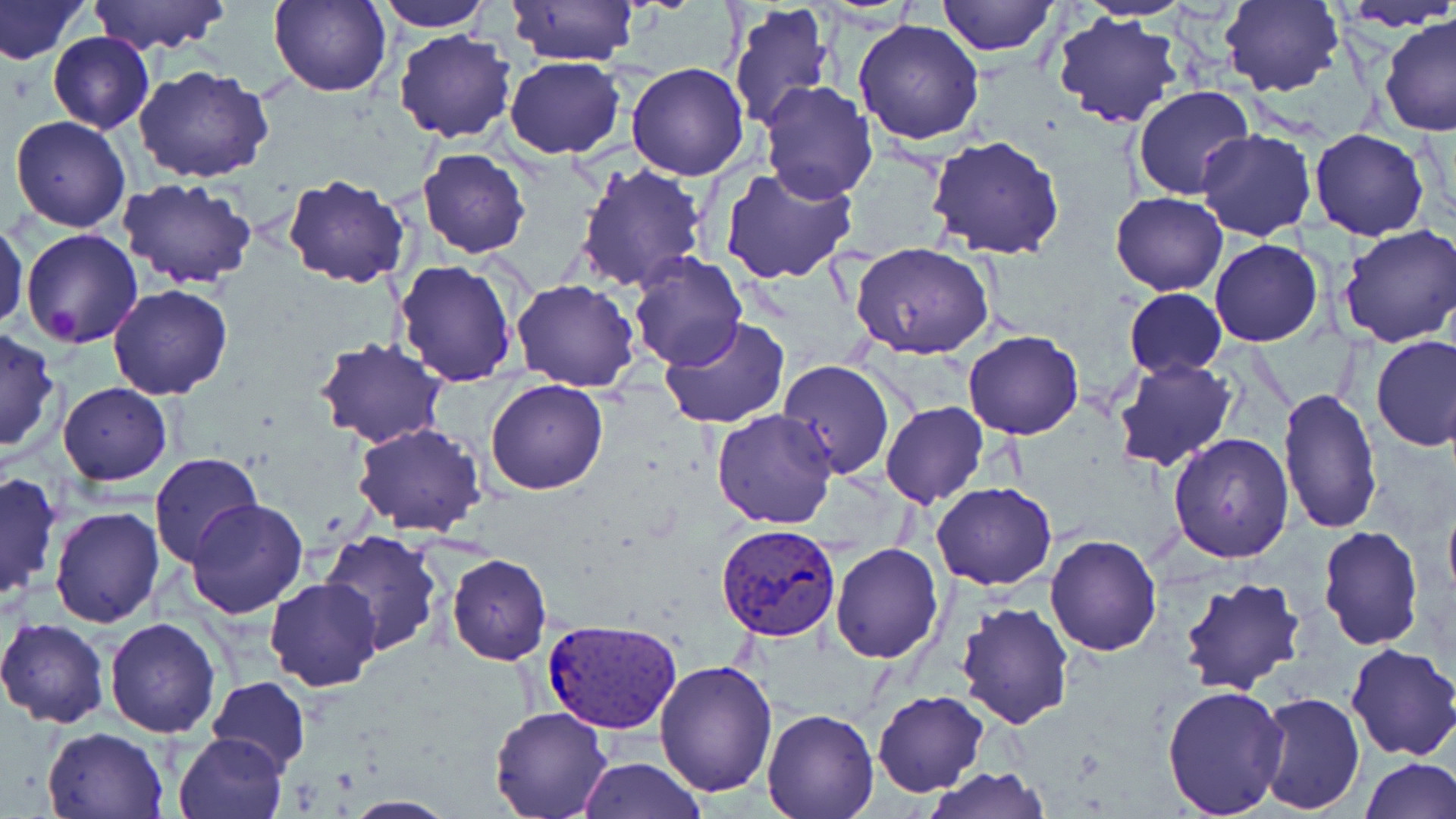
Approximate bounding boxes as [x1, y1, x2, y2] in pixels. Platelet locations: [45, 305, 79, 340]. Plasmodium vivax-infected red blood cell locations: [717, 522, 843, 641], [540, 618, 684, 734]. Uninfected red blood cell locations: [0, 0, 89, 66], [86, 0, 230, 54], [269, 0, 392, 97], [376, 0, 492, 31], [936, 0, 1060, 56], [1080, 0, 1191, 22], [1220, 0, 1345, 99], [1334, 0, 1456, 32], [506, 1, 640, 69], [728, 2, 836, 131], [1051, 11, 1184, 129], [1380, 15, 1455, 137], [852, 19, 984, 145], [394, 30, 519, 144], [49, 32, 155, 134], [503, 55, 627, 159], [625, 63, 750, 182], [133, 65, 276, 183], [758, 81, 879, 203], [1132, 85, 1254, 201], [10, 115, 132, 234], [1309, 128, 1432, 241], [1196, 129, 1318, 242], [926, 135, 1065, 260], [418, 149, 530, 257], [575, 162, 710, 293], [718, 167, 860, 285], [282, 175, 411, 287], [118, 177, 259, 292], [1111, 192, 1226, 295], [599, 193, 743, 346], [0, 219, 28, 334], [1338, 225, 1456, 350], [20, 228, 144, 349], [1210, 238, 1324, 347], [851, 242, 995, 361], [626, 253, 747, 372], [394, 261, 519, 387], [511, 278, 639, 391], [108, 285, 232, 400], [1123, 288, 1226, 377], [658, 317, 790, 429], [0, 326, 62, 455], [962, 330, 1085, 439], [315, 335, 449, 448], [1371, 335, 1456, 451], [1113, 357, 1240, 473], [776, 358, 893, 481], [485, 379, 609, 496], [59, 383, 171, 484], [1277, 387, 1382, 535], [879, 401, 988, 509], [711, 408, 839, 530], [352, 422, 487, 536], [1168, 431, 1295, 562], [149, 453, 263, 569], [0, 469, 62, 603], [930, 481, 1057, 590], [1442, 497, 1456, 611], [187, 499, 309, 619], [49, 505, 163, 628], [1317, 525, 1425, 651], [320, 530, 445, 654], [1045, 535, 1162, 657], [829, 542, 945, 663], [447, 553, 551, 666], [1177, 575, 1309, 697], [264, 577, 382, 691], [954, 601, 1073, 728], [0, 616, 110, 728], [105, 617, 221, 737], [1344, 642, 1456, 761], [655, 659, 778, 797], [205, 675, 310, 772], [1160, 683, 1289, 816], [873, 689, 989, 797], [1252, 691, 1366, 815], [489, 707, 614, 819], [761, 709, 880, 819], [41, 726, 169, 819], [173, 729, 289, 819], [1358, 757, 1455, 818], [578, 758, 704, 819], [923, 767, 1051, 819], [337, 795, 458, 817]. Slide-level diagnosis: Plasmodium vivax. 1000x magnification. May-Grünwald-Giemsa-stained preparation. Light microscopy. Thin blood smear. Image is 1456×819 pixels. Single field of view.